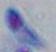

{
  "identification": "Toxoplasma gondii",
  "modality": "photomicrograph",
  "magnification": "1000x"
}